Report the malaria status of this cell.
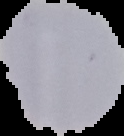

Uninfected.

Image is 124×136 pixels. Segmented cell region on a black background. From a thin blood film.